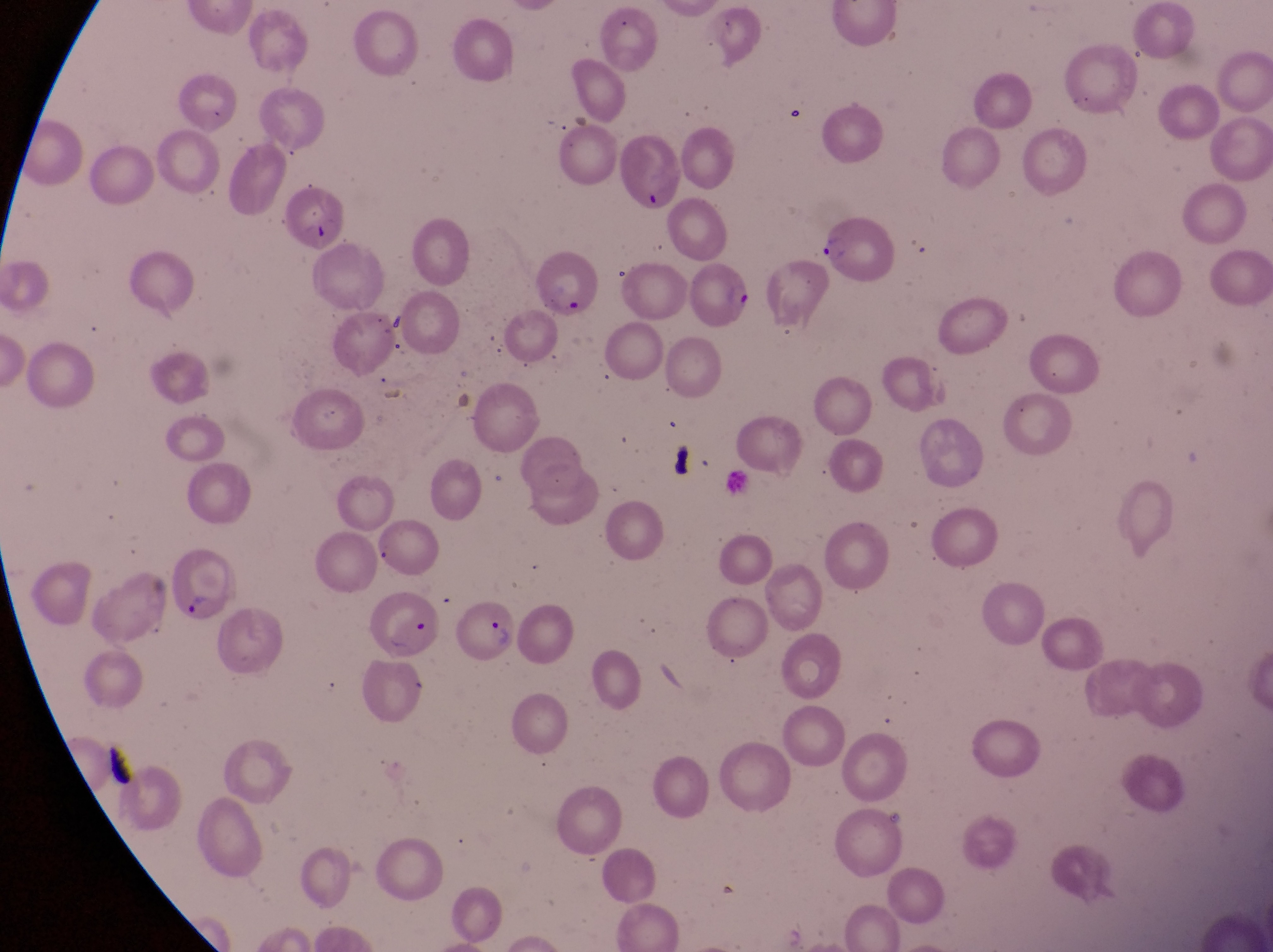
Approximate bounding boxes as {left, top, right, bottom} in pixels.
Summary:
  - Parasitised red blood cell locations: {616, 135, 679, 210}, {282, 190, 349, 250}, {814, 209, 902, 284}, {539, 240, 606, 317}, {688, 262, 754, 329}, {165, 552, 237, 619}, {460, 604, 515, 657}
  - Magnification: 1000x
  - Preparation: thin blood film
  - Country: Uganda
  - Field of view: single
  - Capture: smartphone photograph through the eyepiece of an Olympus CX-23 microscope
  - Image size: 1273×952 pixels